Classify this cell by malaria status.
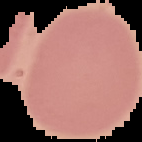

Uninfected.

Summary:
  - Image type: segmented cell region with the area outside set to black
  - Image size: 142×142 pixels
  - Preparation: thin blood film